Identify the cell.
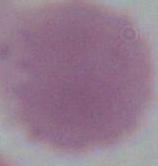
An erythrocyte.

Summary:
  - Modality: micrograph
  - Magnification: 1000x